Identify the preparation type.
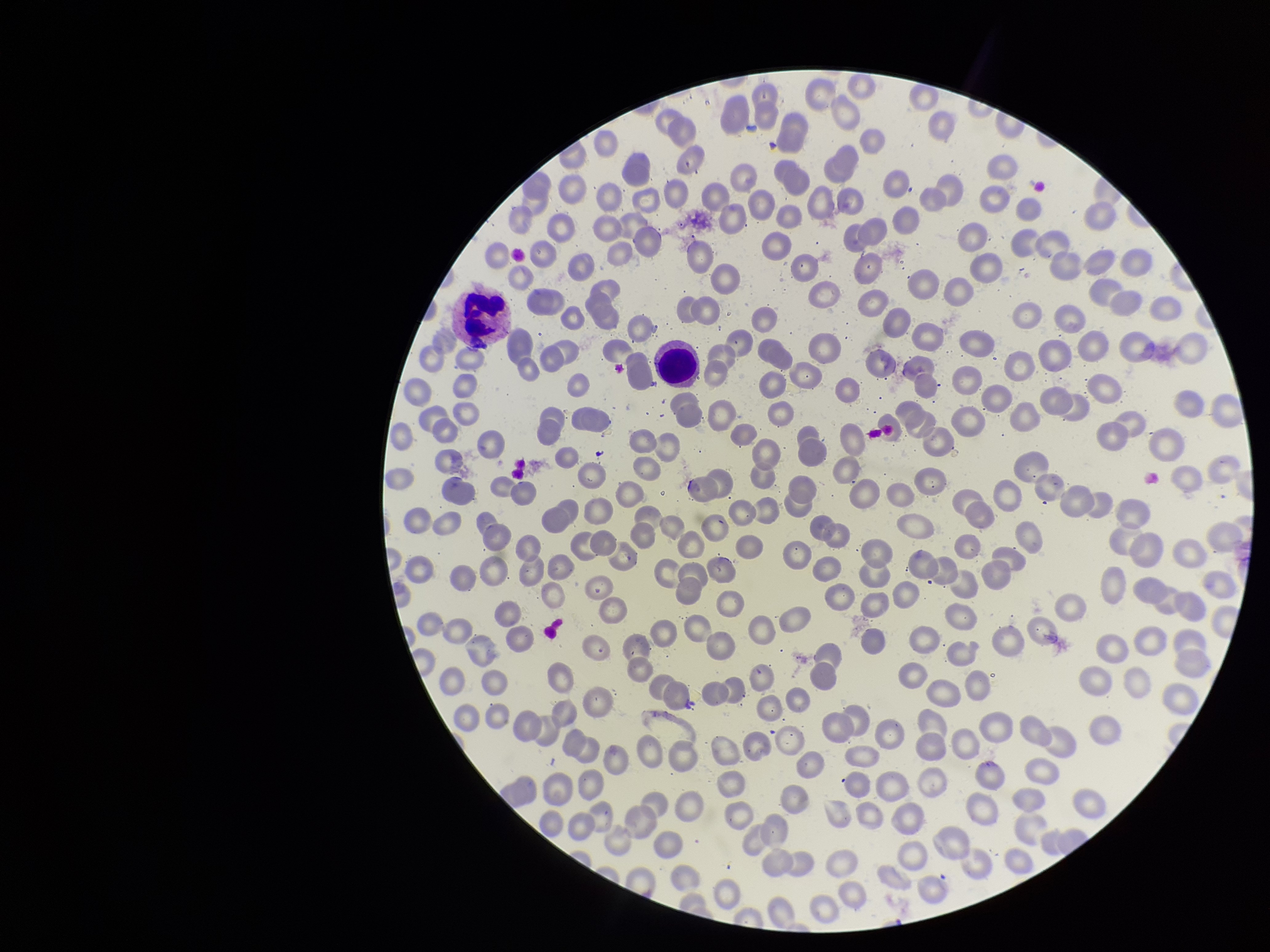
A thin smear.

Single field of view. Giemsa stain. Red blood cell count: 271. Patient malaria status: negative. Parasitized red blood cell count: 0. Image is 1270×952 pixels. Photographed through the microscope eyepiece with a smartphone camera. Parasitized red blood cells: none detected.